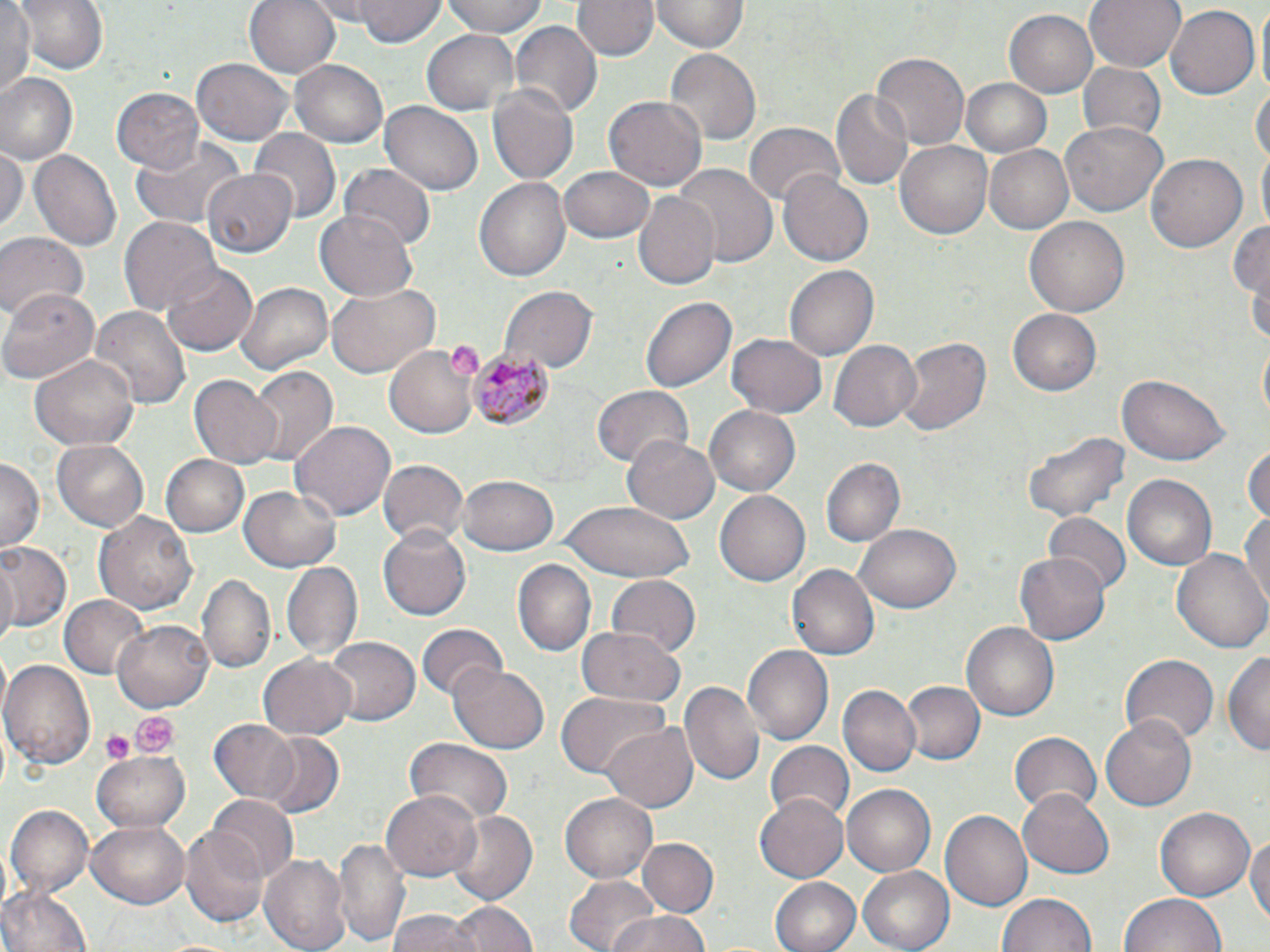
Approximate bounding boxes as [x1, y1, x2, y2] in pixels. Uninfected red blood cell locations: [14, 0, 106, 77], [245, 0, 341, 79], [359, 0, 446, 48], [444, 0, 548, 38], [575, 0, 656, 61], [1085, 0, 1184, 73], [1, 2, 37, 99], [652, 2, 746, 53], [1164, 5, 1259, 101], [1005, 9, 1098, 99], [509, 22, 601, 120], [424, 30, 518, 114], [664, 49, 762, 146], [869, 52, 971, 150], [193, 56, 293, 146], [291, 59, 388, 150], [1076, 63, 1166, 143], [2, 74, 79, 164], [1252, 76, 1269, 177], [961, 77, 1052, 157], [487, 83, 579, 186], [113, 86, 204, 172], [831, 89, 915, 189], [604, 96, 706, 191], [379, 100, 484, 196], [1058, 121, 1168, 219], [742, 124, 844, 209], [249, 127, 339, 221], [129, 136, 242, 231], [895, 136, 993, 237], [983, 144, 1072, 233], [29, 148, 122, 254], [0, 149, 25, 235], [1147, 153, 1247, 253], [671, 164, 777, 271], [340, 165, 435, 251], [557, 165, 656, 243], [200, 171, 293, 258], [776, 171, 873, 266], [474, 175, 572, 284], [632, 193, 720, 290], [314, 213, 419, 300], [118, 216, 221, 320], [1023, 217, 1131, 320], [1229, 218, 1269, 299], [0, 234, 84, 325], [162, 264, 256, 355], [785, 264, 877, 361], [233, 280, 335, 376], [327, 282, 440, 377], [0, 285, 101, 384], [499, 287, 596, 376], [642, 294, 737, 394], [89, 305, 190, 413], [1008, 308, 1102, 397], [895, 333, 992, 440], [726, 334, 827, 417], [829, 338, 921, 432], [385, 343, 480, 438], [30, 351, 139, 451], [247, 368, 338, 468], [190, 374, 281, 467], [1117, 374, 1231, 466], [591, 386, 691, 468], [705, 406, 800, 498], [289, 420, 395, 523], [1023, 429, 1130, 522], [622, 434, 720, 526], [52, 439, 150, 531], [1246, 442, 1270, 526], [161, 453, 250, 538], [0, 457, 42, 552], [819, 457, 906, 548], [377, 460, 466, 548], [1120, 472, 1216, 570], [458, 474, 560, 556], [239, 486, 345, 573], [715, 491, 811, 586], [560, 500, 697, 581], [94, 511, 197, 616], [1240, 511, 1270, 602], [1042, 513, 1132, 595], [856, 523, 964, 613], [378, 528, 470, 621], [0, 540, 72, 635], [1171, 547, 1270, 655], [1016, 550, 1111, 645], [280, 561, 363, 660], [514, 561, 596, 658], [786, 564, 879, 661], [197, 574, 276, 675], [607, 575, 701, 659], [59, 593, 150, 678], [114, 616, 215, 711], [962, 622, 1059, 722], [417, 623, 508, 702], [575, 627, 685, 707], [324, 636, 419, 726], [741, 644, 832, 746], [1225, 647, 1270, 758], [1119, 652, 1218, 747], [259, 654, 356, 740], [2, 660, 95, 766], [448, 662, 548, 754], [900, 679, 985, 768], [679, 681, 765, 788], [836, 685, 921, 778], [556, 692, 672, 780], [1101, 711, 1198, 809], [210, 719, 303, 803], [603, 722, 697, 811], [1010, 730, 1102, 815], [258, 736, 345, 817], [404, 738, 514, 825], [765, 742, 853, 825], [93, 751, 190, 832], [843, 783, 939, 877], [1019, 787, 1114, 879], [383, 788, 481, 881], [559, 792, 658, 883], [755, 792, 849, 884], [208, 795, 297, 880], [6, 805, 92, 896], [1152, 805, 1256, 903], [448, 811, 537, 907], [943, 811, 1031, 909], [87, 818, 189, 908], [181, 826, 270, 928], [1246, 830, 1270, 931], [333, 833, 411, 948], [638, 838, 716, 917], [261, 851, 351, 952], [859, 865, 958, 952], [564, 874, 662, 952], [770, 876, 861, 952], [0, 884, 91, 952], [997, 892, 1098, 952], [1120, 892, 1228, 952], [446, 903, 535, 952], [388, 911, 475, 952], [601, 912, 717, 952]. Platelet locations: [451, 342, 485, 379], [129, 711, 175, 758], [100, 731, 133, 764]. Plasmodium malariae-infected red blood cell locations: [468, 348, 555, 429]. Slide-level diagnosis: Plasmodium malariae. May-Grünwald-Giemsa stain. Single field of view. Light microscopy. Captured at 1000x magnification. Image is 1270×952 pixels. Thin blood film.